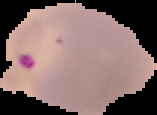
malaria status = parasitized
image type = cell region segmented out of the field of view; surrounding area masked to black
image size = 157×115 pixels
preparation = thin blood film